Locate every Plasmodium ovale-infected red blood cell.
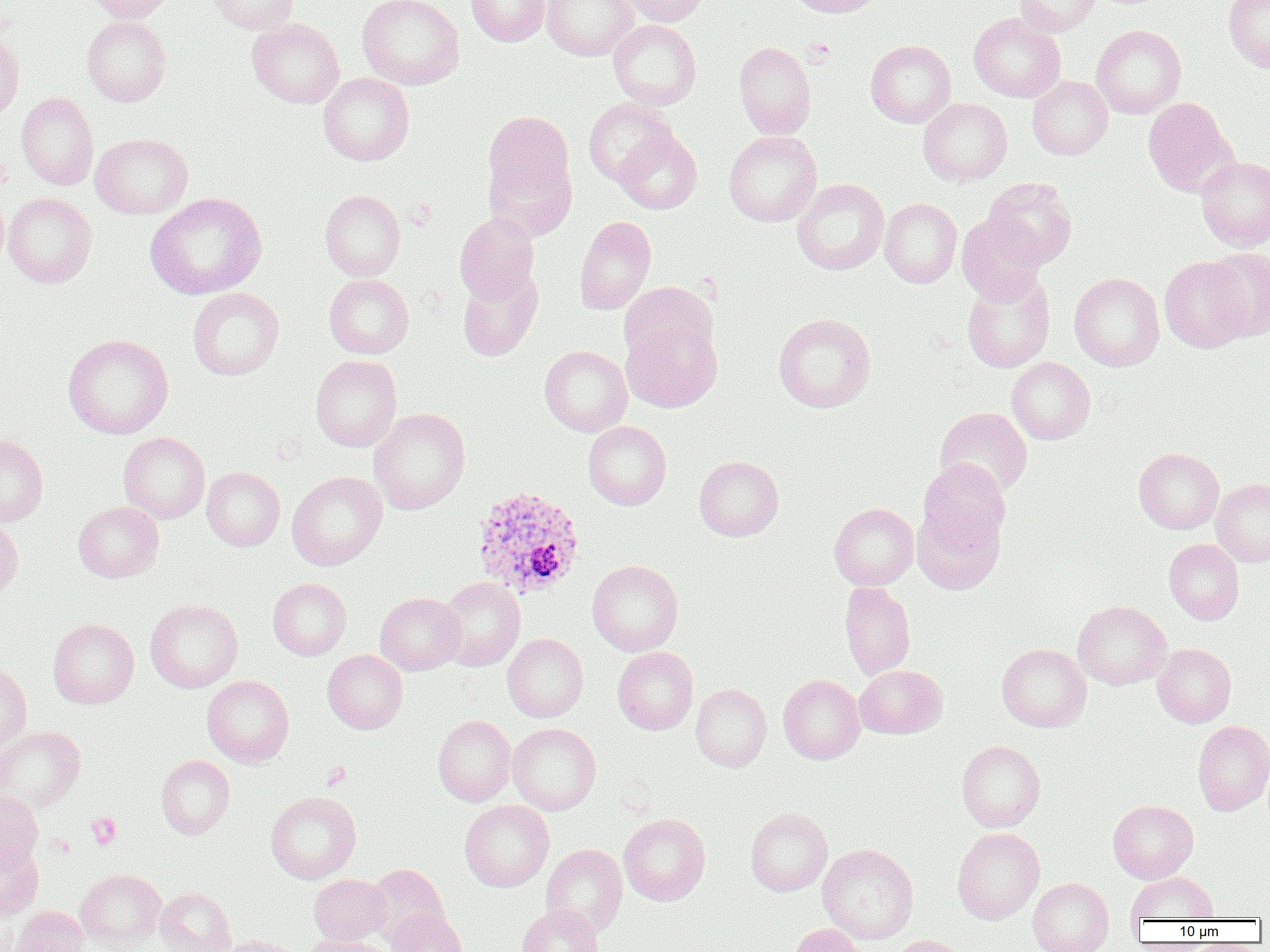

Approximate bounding boxes as (x1,y1)-(x2,y2) corner pairs in pixels.
Plasmodium ovale-infected red blood cells: (471,485)-(585,599).

Summary:
  - Platelet locations: (802,38)-(835,64), (322,762)-(351,788), (86,813)-(121,849)
  - Uninfected red blood cell locations: (85,0)-(178,22), (209,0)-(300,34), (357,0)-(464,90), (465,0)-(550,47), (541,0)-(637,61), (615,0)-(709,26), (785,0)-(887,17), (1014,0)-(1103,35), (1223,0)-(1270,73), (968,12)-(1065,102), (82,15)-(171,106), (247,18)-(344,108), (608,19)-(702,110), (1091,25)-(1186,118), (0,30)-(25,120), (866,39)-(956,128), (733,41)-(816,138), (318,73)-(414,165), (1027,76)-(1113,160), (16,92)-(99,189), (1143,97)-(1237,197), (583,98)-(677,186), (918,98)-(1012,186), (483,110)-(574,204), (614,127)-(702,214), (723,130)-(822,226), (90,133)-(193,219), (484,155)-(576,240), (1196,156)-(1270,251), (983,177)-(1078,270), (791,179)-(889,275), (320,190)-(405,280), (3,192)-(97,287), (145,193)-(267,299), (880,198)-(962,288), (454,212)-(539,304), (956,212)-(1046,304), (574,216)-(656,314), (1203,247)-(1270,340), (1159,256)-(1253,352), (457,268)-(542,362), (961,271)-(1055,373), (1069,272)-(1165,371), (324,273)-(414,359), (619,282)-(718,367), (187,287)-(284,380), (773,313)-(876,412), (621,315)-(722,413), (62,334)-(174,439), (539,345)-(632,436), (310,355)-(402,451), (1007,357)-(1095,444), (369,407)-(470,514), (935,407)-(1032,497), (583,421)-(671,510), (118,431)-(210,523), (0,433)-(48,526), (1133,447)-(1224,534), (694,456)-(784,541), (918,458)-(1011,549), (202,466)-(284,551), (286,471)-(387,570), (1211,479)-(1270,567), (73,501)-(163,582), (829,502)-(918,591), (913,505)-(1005,595), (0,518)-(23,604), (1164,538)-(1244,624), (586,559)-(683,656), (438,577)-(525,671), (267,578)-(351,660), (839,582)-(915,680), (375,592)-(466,675), (145,599)-(243,692), (1073,601)-(1171,689), (48,618)-(138,708), (502,633)-(588,722), (996,643)-(1091,732), (1152,644)-(1236,727), (612,647)-(698,735), (323,650)-(408,734), (0,661)-(31,749), (854,665)-(947,739), (778,674)-(865,764), (202,675)-(294,767), (691,683)-(772,772), (433,715)-(516,807), (1193,720)-(1270,815), (508,723)-(601,814), (0,725)-(85,814), (956,740)-(1045,832), (156,754)-(234,839), (0,791)-(42,869), (265,791)-(361,884), (459,800)-(554,892), (1108,800)-(1199,883), (745,807)-(832,896), (619,813)-(710,905), (952,827)-(1044,924), (0,842)-(43,919), (541,843)-(627,936), (817,843)-(919,943), (365,864)-(449,946), (75,868)-(167,950), (1126,871)-(1219,922), (309,874)-(389,946), (1028,877)-(1114,952), (155,887)-(236,952), (517,904)-(602,952), (9,905)-(88,952), (385,909)-(468,952), (790,924)-(867,952), (212,934)-(300,952), (302,935)-(394,952), (888,935)-(971,952)
  - Slide-level diagnosis: Plasmodium ovale
  - Field of view: one of a larger specimen
  - Modality: optical microscopy
  - Image size: 1270×952 pixels
  - Magnification: 1000x
  - Preparation: thin blood smear